Classify this cell by malaria status.
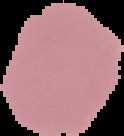

It is uninfected.

Summary:
  - Image size: 124×136 pixels
  - Preparation: thin blood film
  - Image type: cell region segmented out of the field of view; surrounding area masked to black